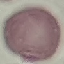
{
  "malaria_status": "uninfected",
  "stain": "Giemsa",
  "image_type": "cell patch, automatically extracted from a larger field of view and resized to 64 × 64 pixels",
  "capture": "smartphone through the microscope eyepiece",
  "preparation": "thin blood smear"
}